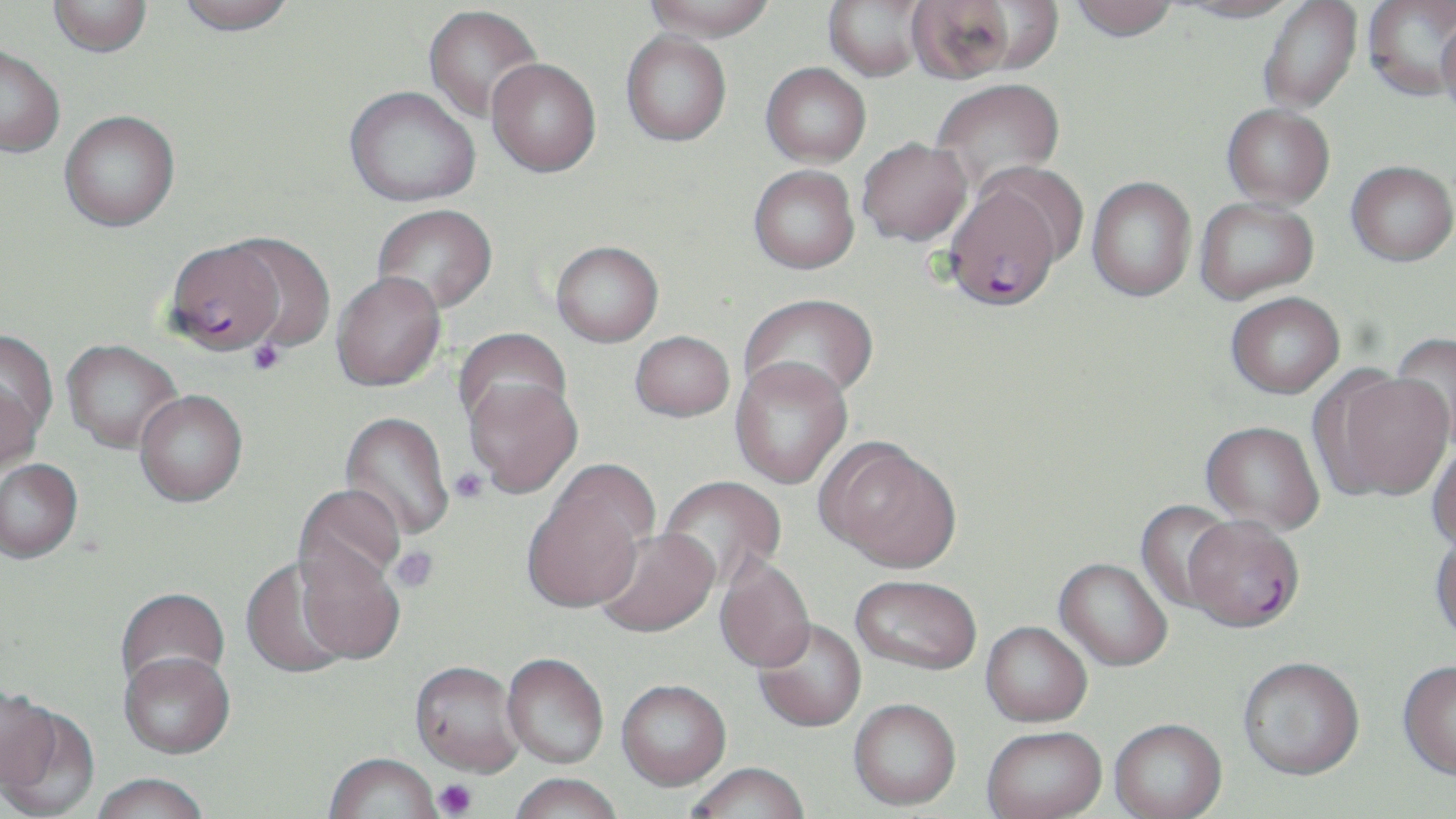 Approximate bounding boxes as (x1,y1)-(x2,y2) corner pairs in pixels. Plasmodium falciparum-infected red blood cell locations: (943,184)-(1062,310), (164,239)-(284,354), (1183,520)-(1304,637). Uninfected red blood cell locations: (176,0)-(295,35), (645,0)-(775,42), (823,0)-(929,80), (904,0)-(1027,83), (1068,0)-(1180,41), (1175,0)-(1303,23), (1257,0)-(1362,114), (48,1)-(153,57), (1363,1)-(1455,100), (423,5)-(543,123), (1436,14)-(1456,121), (621,31)-(731,146), (0,45)-(65,157), (486,58)-(600,177), (761,62)-(871,167), (930,78)-(1065,193), (344,85)-(480,206), (1222,104)-(1335,209), (59,110)-(180,232), (857,138)-(972,246), (1346,160)-(1456,266), (974,162)-(1090,269), (748,165)-(859,273), (1086,176)-(1196,301), (1194,197)-(1319,304), (372,203)-(498,313), (224,233)-(336,352), (551,240)-(663,347), (330,270)-(446,391), (740,293)-(878,404), (1225,294)-(1345,400), (454,328)-(573,436), (629,330)-(734,422), (0,332)-(56,462), (1388,332)-(1456,451), (61,339)-(182,453), (730,358)-(853,489), (1313,369)-(1453,504), (463,375)-(583,497), (134,389)-(248,507), (339,411)-(454,543), (1200,424)-(1324,537), (818,440)-(962,574), (1427,443)-(1456,555), (0,459)-(83,566), (658,476)-(786,593), (522,480)-(648,617), (293,484)-(406,594), (1135,501)-(1239,614), (594,529)-(720,641), (1430,534)-(1456,649), (294,542)-(406,667), (239,556)-(355,680), (714,557)-(816,676), (1053,560)-(1172,673), (850,578)-(980,678), (115,589)-(230,698), (752,621)-(866,734), (980,624)-(1092,729), (119,655)-(235,763), (501,656)-(608,771), (1238,661)-(1364,784), (409,664)-(525,781), (1397,664)-(1456,784), (616,683)-(731,794), (0,685)-(58,793), (848,702)-(961,813), (1,707)-(100,819), (1109,722)-(1228,819), (982,729)-(1107,819), (324,756)-(441,819), (686,766)-(811,819), (89,777)-(210,819), (509,777)-(622,819). Platelet locations: (247,340)-(287,376), (450,467)-(488,503), (390,546)-(438,593), (434,779)-(477,818). Slide-level diagnosis: Plasmodium falciparum. One field of a larger specimen. May-Grünwald-Giemsa-stained preparation. Captured at 1000x magnification. Optical microscopy. Image is 1456×819 pixels. Thin blood smear.